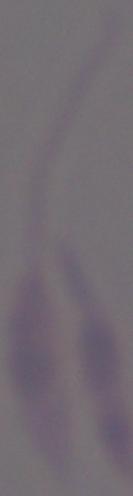
identification = Leishmania
modality = micrograph
magnification = 1000x